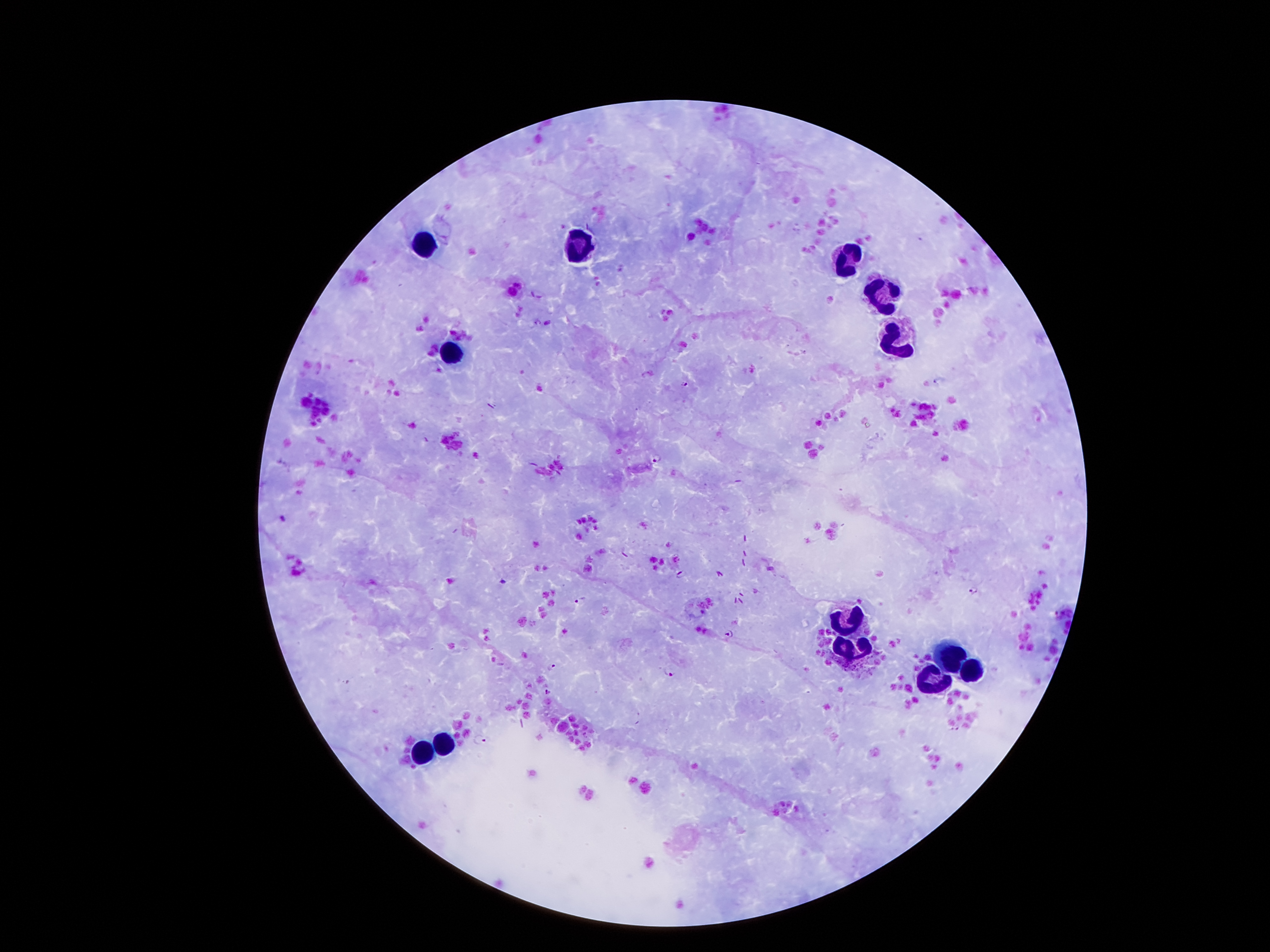
Approximate centers as {x, y} in pixels. Malaria parasite locations: {686, 384}, {657, 458}, {283, 519}, {682, 574}, {503, 582}, {973, 589}, {580, 600}, {1058, 614}, {730, 634}, {552, 667}, {670, 672}, {956, 728}, {480, 740}. Leukocyte locations: {418, 248}, {579, 250}, {852, 255}, {879, 295}, {895, 334}, {452, 359}, {840, 626}, {852, 646}, {945, 655}, {979, 674}, {929, 683}, {438, 746}, {418, 756}. Single field of view. Patient malaria status: infected with Plasmodium falciparum. 100x magnification. Thick blood smear. Giemsa stain. Smartphone photograph taken through the microscope eyepiece. Image is 1270×952 pixels.